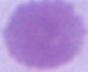

An erythrocyte is seen. Photomicrograph. 1000x magnification.